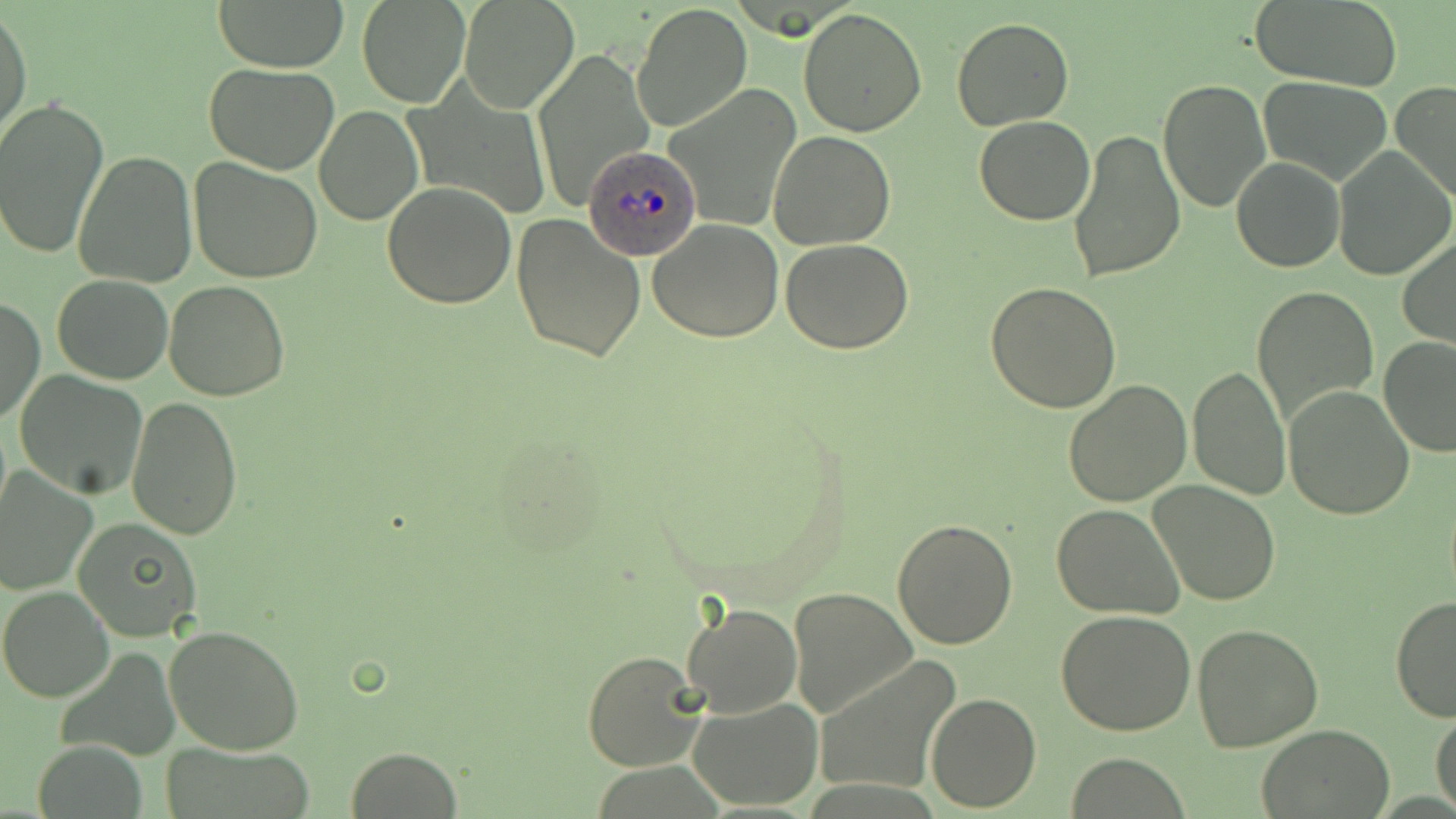 Approximate bounding boxes as (x1,y1)-(x2,y2) corner pairs in pixels. Uninfected red blood cell locations: (210,0)-(349,72), (356,0)-(471,109), (1249,0)-(1403,89), (459,1)-(578,114), (630,2)-(753,135), (0,7)-(33,148), (797,8)-(929,137), (951,18)-(1074,131), (531,49)-(654,208), (203,62)-(339,173), (1259,76)-(1394,186), (1158,78)-(1269,211), (1391,82)-(1456,206), (665,85)-(803,233), (0,95)-(109,260), (313,105)-(423,225), (975,116)-(1095,226), (1066,127)-(1186,284), (767,130)-(895,250), (1333,146)-(1454,282), (73,150)-(198,288), (189,157)-(324,284), (1231,157)-(1344,272), (383,181)-(516,308), (511,214)-(645,362), (647,218)-(784,343), (1397,234)-(1456,350), (779,237)-(916,353), (51,274)-(175,384), (164,281)-(291,403), (984,282)-(1121,412), (1251,284)-(1380,429), (1,298)-(45,426), (1376,336)-(1456,457), (1189,362)-(1292,502), (14,370)-(149,498), (1061,379)-(1191,505), (1284,384)-(1415,520), (127,396)-(243,540), (0,471)-(98,593), (1150,481)-(1281,605), (2,491)-(168,619), (1051,503)-(1185,619), (73,518)-(201,642), (893,519)-(1018,649), (0,585)-(114,703), (789,586)-(917,722), (1390,594)-(1456,724), (681,602)-(802,718), (1056,609)-(1198,737), (1193,623)-(1324,752), (165,625)-(306,754), (582,650)-(707,771), (814,656)-(960,796), (926,691)-(1041,811), (688,695)-(822,808), (1431,706)-(1456,814), (1255,725)-(1396,819), (34,741)-(147,819), (162,742)-(318,818), (346,747)-(463,819), (1068,753)-(1190,817). Plasmodium ovale-infected red blood cell locations: (583,143)-(700,262). Slide-level diagnosis: Plasmodium ovale. 1000x magnification. Image is 1456×819 pixels. Thin blood smear. Single field of view. May-Grünwald-Giemsa-stained preparation. Optical microscopy.